Locate every Trypanosoma brucei.
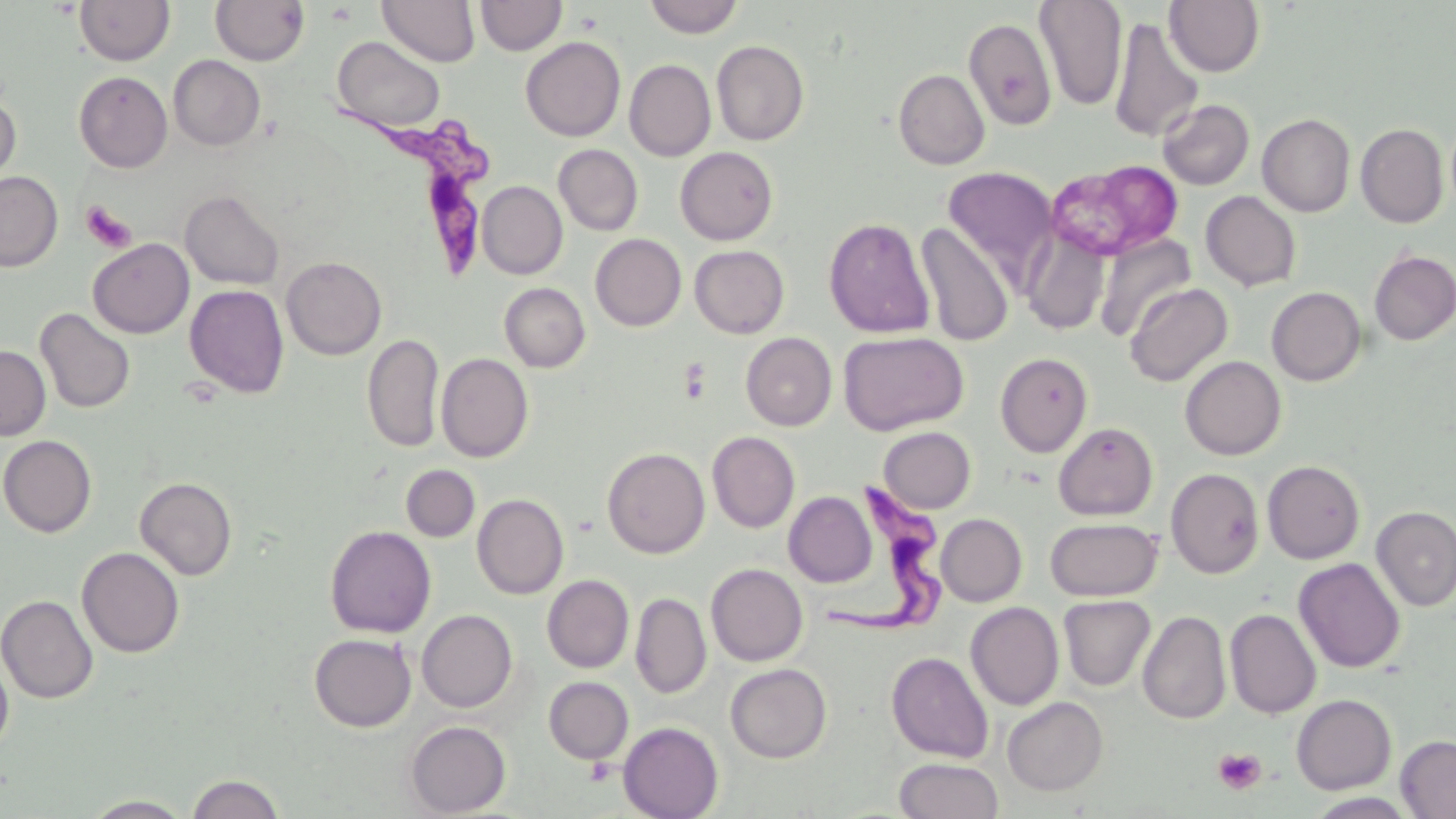

Approximate bounding boxes as named x1/y1/x2/y2 corners in pixels.
Trypanosoma brucei: (x1=336, y1=97, x2=503, y2=277), (x1=818, y1=473, x2=957, y2=636).

Summary:
  - Platelet locations: (x1=80, y1=201, x2=136, y2=253), (x1=679, y1=358, x2=713, y2=404), (x1=1212, y1=748, x2=1266, y2=795)
  - Uninfected red blood cell locations: (x1=74, y1=0, x2=174, y2=66), (x1=377, y1=0, x2=480, y2=67), (x1=475, y1=0, x2=566, y2=56), (x1=643, y1=0, x2=744, y2=38), (x1=1034, y1=0, x2=1128, y2=111), (x1=1164, y1=0, x2=1265, y2=76), (x1=210, y1=1, x2=309, y2=66), (x1=1109, y1=16, x2=1204, y2=142), (x1=963, y1=17, x2=1057, y2=130), (x1=520, y1=36, x2=625, y2=141), (x1=332, y1=37, x2=445, y2=133), (x1=711, y1=40, x2=809, y2=145), (x1=168, y1=55, x2=265, y2=151), (x1=624, y1=59, x2=716, y2=161), (x1=894, y1=68, x2=990, y2=170), (x1=73, y1=71, x2=172, y2=172), (x1=0, y1=94, x2=21, y2=190), (x1=1158, y1=99, x2=1254, y2=190), (x1=1258, y1=113, x2=1355, y2=217), (x1=1356, y1=123, x2=1448, y2=228), (x1=554, y1=144, x2=643, y2=235), (x1=675, y1=146, x2=778, y2=245), (x1=1046, y1=160, x2=1183, y2=261), (x1=943, y1=167, x2=1057, y2=284), (x1=0, y1=171, x2=63, y2=272), (x1=477, y1=181, x2=567, y2=279), (x1=180, y1=189, x2=285, y2=290), (x1=1200, y1=191, x2=1301, y2=291), (x1=823, y1=217, x2=935, y2=338), (x1=916, y1=222, x2=1015, y2=346), (x1=1021, y1=226, x2=1111, y2=336), (x1=590, y1=233, x2=686, y2=331), (x1=1096, y1=234, x2=1196, y2=341), (x1=88, y1=238, x2=194, y2=338), (x1=690, y1=245, x2=789, y2=338), (x1=1369, y1=249, x2=1456, y2=345), (x1=282, y1=256, x2=386, y2=360), (x1=499, y1=282, x2=590, y2=372), (x1=1124, y1=282, x2=1232, y2=387), (x1=184, y1=284, x2=289, y2=398), (x1=1266, y1=286, x2=1366, y2=386), (x1=34, y1=307, x2=135, y2=414), (x1=838, y1=331, x2=968, y2=435), (x1=741, y1=332, x2=837, y2=430), (x1=362, y1=333, x2=444, y2=453), (x1=0, y1=345, x2=51, y2=440), (x1=995, y1=352, x2=1093, y2=457), (x1=436, y1=353, x2=533, y2=462), (x1=1180, y1=355, x2=1286, y2=460), (x1=1053, y1=422, x2=1158, y2=520), (x1=878, y1=426, x2=976, y2=513), (x1=707, y1=431, x2=800, y2=533), (x1=0, y1=435, x2=97, y2=537), (x1=602, y1=447, x2=710, y2=558), (x1=1262, y1=460, x2=1365, y2=564), (x1=401, y1=465, x2=480, y2=542), (x1=1166, y1=468, x2=1264, y2=578), (x1=135, y1=477, x2=237, y2=580), (x1=784, y1=491, x2=876, y2=587), (x1=472, y1=493, x2=568, y2=599), (x1=1371, y1=505, x2=1456, y2=611), (x1=936, y1=513, x2=1027, y2=606), (x1=1045, y1=517, x2=1162, y2=601), (x1=324, y1=525, x2=436, y2=638), (x1=76, y1=547, x2=185, y2=658), (x1=1293, y1=557, x2=1405, y2=673), (x1=706, y1=563, x2=807, y2=666), (x1=542, y1=575, x2=634, y2=673), (x1=631, y1=593, x2=711, y2=698), (x1=0, y1=595, x2=98, y2=704), (x1=1058, y1=595, x2=1155, y2=691), (x1=965, y1=602, x2=1064, y2=710), (x1=417, y1=609, x2=517, y2=712), (x1=1225, y1=609, x2=1321, y2=719), (x1=1138, y1=610, x2=1231, y2=724), (x1=309, y1=633, x2=416, y2=732), (x1=886, y1=651, x2=994, y2=763), (x1=0, y1=655, x2=14, y2=756), (x1=725, y1=663, x2=832, y2=763), (x1=543, y1=676, x2=633, y2=764), (x1=1291, y1=694, x2=1396, y2=794), (x1=1002, y1=696, x2=1108, y2=796), (x1=405, y1=720, x2=511, y2=817), (x1=618, y1=722, x2=724, y2=819), (x1=1396, y1=735, x2=1456, y2=818), (x1=894, y1=758, x2=1004, y2=819), (x1=186, y1=773, x2=285, y2=819), (x1=1306, y1=793, x2=1417, y2=819), (x1=82, y1=795, x2=195, y2=818)
  - Slide-level diagnosis: Trypanosoma brucei
  - Preparation: thin blood film
  - Field of view: single
  - Modality: optical microscopy
  - Image size: 1456×819 pixels
  - Magnification: 1000x
  - Stain: May-Grünwald-Giemsa